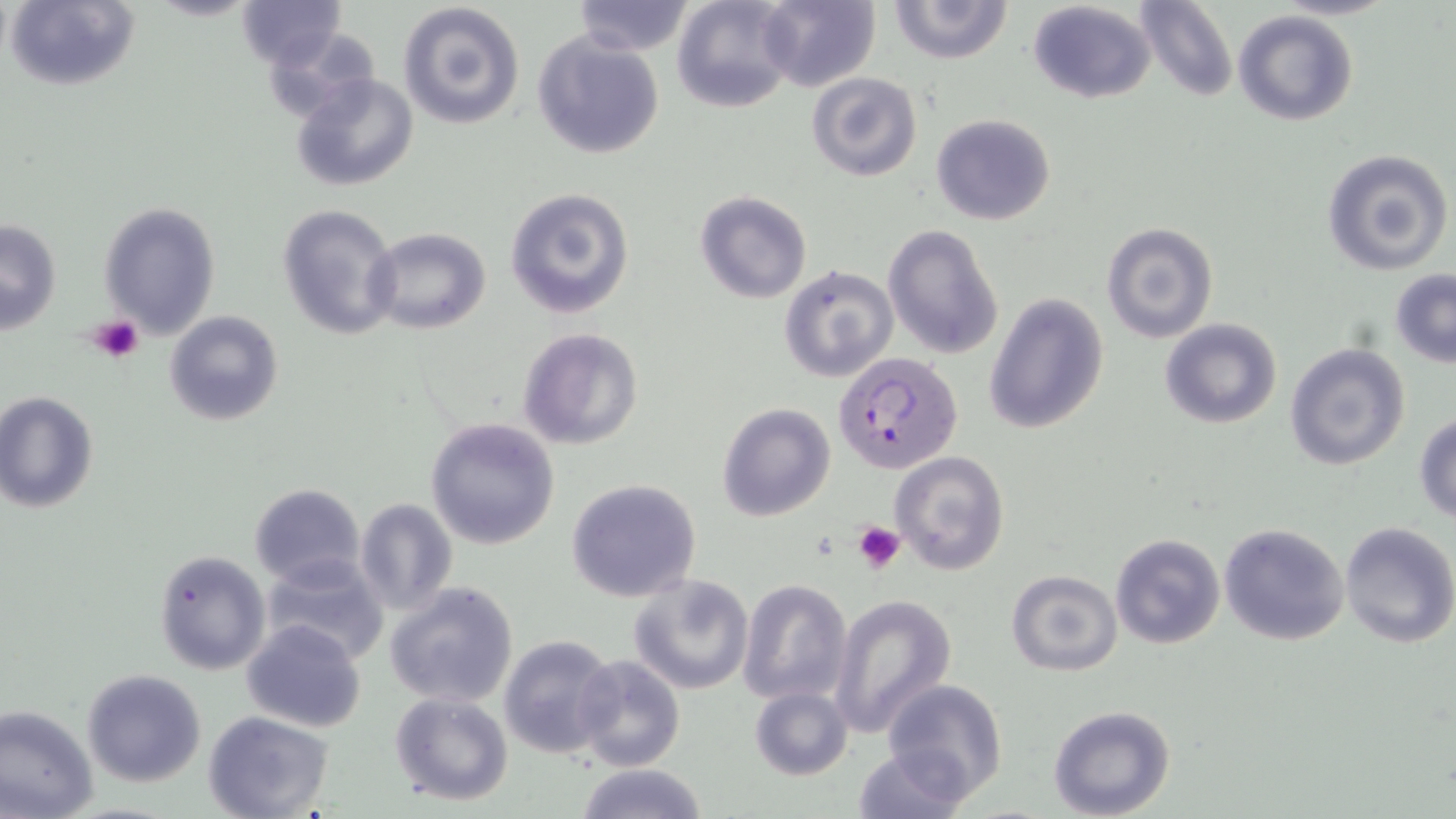
Summary:
  - Coordinate format: approximate bounding boxes as (x1, y1, x2, y2) in pixels
  - Plasmodium falciparum-infected red blood cell locations: (835, 352, 965, 475)
  - Uninfected red blood cell locations: (6, 0, 141, 91), (570, 0, 696, 55), (670, 0, 798, 114), (755, 0, 880, 91), (887, 0, 1015, 64), (1135, 0, 1237, 101), (236, 1, 346, 69), (1027, 1, 1159, 105), (396, 2, 525, 131), (1234, 10, 1358, 126), (262, 24, 379, 124), (532, 31, 665, 160), (806, 72, 923, 181), (292, 73, 419, 191), (931, 114, 1056, 225), (1322, 148, 1453, 277), (505, 187, 634, 319), (695, 190, 813, 304), (98, 201, 221, 340), (276, 203, 401, 339), (1, 217, 62, 335), (1099, 220, 1219, 345), (883, 224, 1004, 361), (366, 228, 491, 335), (779, 264, 900, 384), (1390, 270, 1456, 368), (985, 292, 1109, 435), (163, 309, 285, 427), (1159, 318, 1282, 429), (517, 326, 644, 450), (1283, 342, 1411, 471), (0, 390, 99, 514), (717, 402, 835, 520), (1414, 412, 1456, 523), (426, 417, 560, 550), (890, 450, 1011, 576), (566, 479, 701, 604), (249, 483, 365, 587), (353, 498, 460, 619), (1338, 521, 1456, 649), (1218, 522, 1348, 645), (1109, 533, 1227, 650), (152, 550, 269, 676), (259, 554, 391, 665), (1006, 569, 1122, 675), (628, 574, 756, 695), (736, 578, 852, 705), (386, 581, 519, 708), (830, 594, 957, 736), (240, 620, 366, 734), (498, 634, 617, 759), (574, 654, 684, 771), (80, 669, 206, 787), (883, 678, 1008, 801), (750, 686, 853, 781), (389, 692, 514, 807), (0, 703, 99, 819), (1049, 706, 1176, 819), (205, 711, 334, 819), (854, 744, 973, 818), (573, 763, 708, 819)
  - Platelet locations: (87, 315, 144, 363), (854, 522, 905, 574)
  - Slide-level diagnosis: Plasmodium falciparum
  - Image size: 1456×819 pixels
  - Preparation: thin blood film
  - Modality: light microscopy
  - Stain: May-Grünwald-Giemsa
  - Field of view: one of a larger specimen
  - Magnification: 1000x